Classify this cell by malaria status.
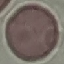
It is uninfected.

Summary:
  - Capture: smartphone through the microscope eyepiece
  - Image type: automatically extracted cell patch, resized to 64 × 64 pixels
  - Preparation: thin blood smear
  - Stain: Giemsa